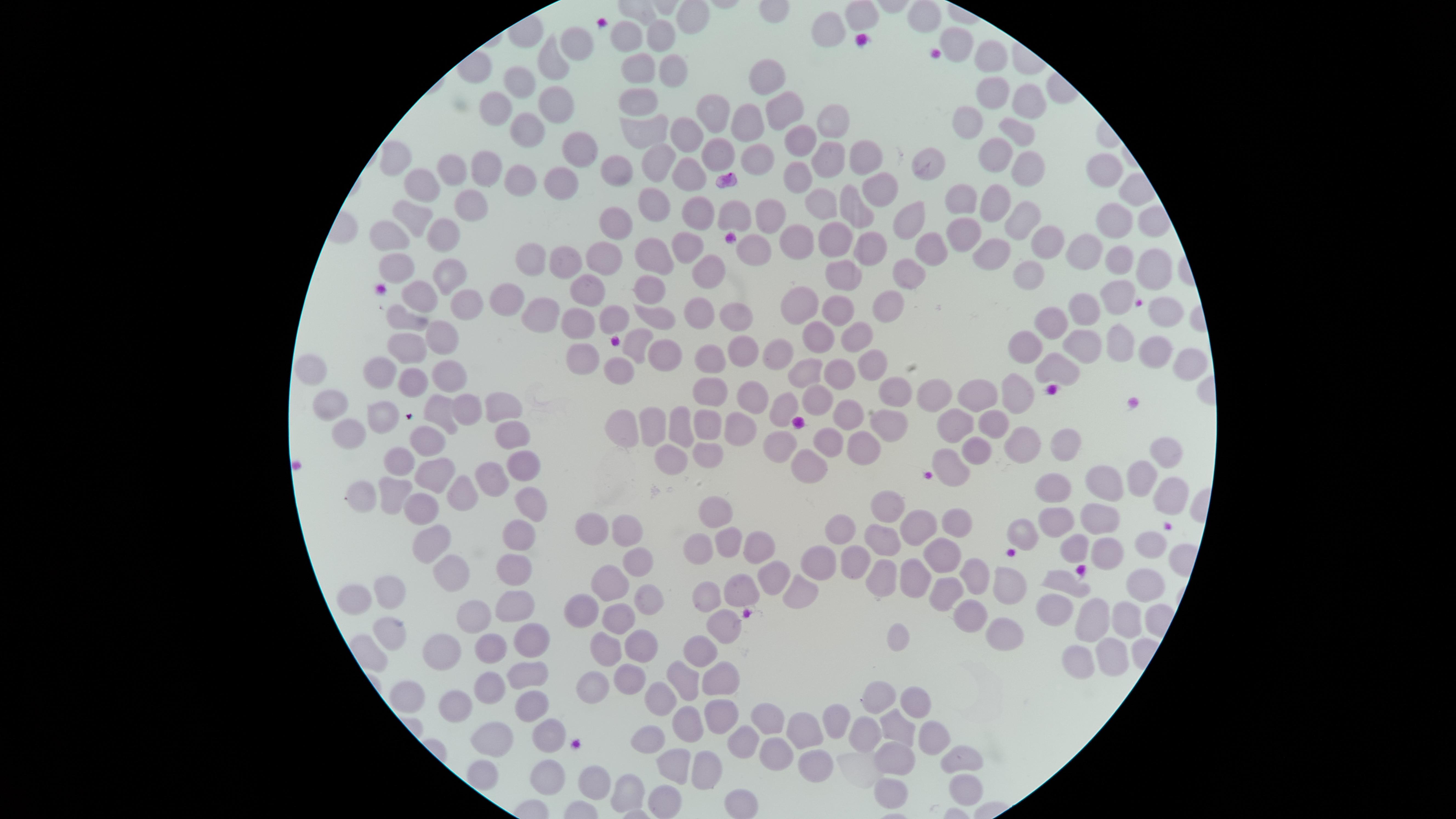

Approximate marker points, in pixels from the top-left corner. Uninfected RBCs: (x=860, y=16), (x=925, y=16), (x=663, y=37), (x=831, y=37), (x=633, y=38), (x=578, y=39), (x=958, y=40), (x=1004, y=50), (x=550, y=64), (x=641, y=67), (x=672, y=68), (x=771, y=79), (x=521, y=83), (x=992, y=91), (x=644, y=96), (x=548, y=103), (x=1030, y=103), (x=782, y=107), (x=495, y=110), (x=707, y=111), (x=828, y=118), (x=970, y=122), (x=743, y=123), (x=643, y=124), (x=686, y=127), (x=527, y=132), (x=1021, y=133), (x=797, y=144), (x=574, y=151), (x=861, y=154), (x=712, y=156), (x=991, y=156), (x=391, y=159), (x=825, y=159), (x=754, y=160), (x=482, y=162), (x=611, y=165), (x=661, y=165), (x=1027, y=165), (x=930, y=168), (x=1106, y=171), (x=447, y=173), (x=689, y=180), (x=793, y=181), (x=518, y=183), (x=561, y=189), (x=876, y=189), (x=421, y=190), (x=959, y=196), (x=654, y=200), (x=992, y=201), (x=819, y=204), (x=470, y=206), (x=696, y=210), (x=736, y=211), (x=855, y=212), (x=767, y=215), (x=418, y=218), (x=1014, y=218), (x=912, y=219), (x=611, y=223), (x=1114, y=227), (x=963, y=230), (x=833, y=237), (x=385, y=239), (x=439, y=239), (x=799, y=239), (x=1046, y=246), (x=686, y=247), (x=934, y=249), (x=1078, y=250), (x=865, y=251), (x=746, y=253), (x=992, y=253), (x=604, y=255), (x=1116, y=259), (x=652, y=260), (x=532, y=261), (x=563, y=262), (x=1153, y=268), (x=391, y=269), (x=910, y=271), (x=712, y=272), (x=444, y=274), (x=1027, y=274), (x=846, y=277), (x=650, y=285), (x=588, y=288), (x=1119, y=296), (x=420, y=299), (x=509, y=300), (x=464, y=301), (x=890, y=302), (x=798, y=306), (x=1089, y=306), (x=700, y=310), (x=837, y=310), (x=1166, y=310), (x=541, y=313), (x=403, y=318), (x=732, y=318), (x=657, y=319), (x=577, y=321), (x=1052, y=322), (x=820, y=336), (x=857, y=337), (x=441, y=340), (x=1122, y=342), (x=1089, y=343), (x=1026, y=344), (x=632, y=346), (x=406, y=348), (x=740, y=352), (x=665, y=356), (x=1154, y=356), (x=774, y=357), (x=710, y=358), (x=580, y=362), (x=1188, y=362), (x=1050, y=366), (x=378, y=368), (x=307, y=369), (x=875, y=369), (x=802, y=370), (x=620, y=373), (x=450, y=375), (x=843, y=376), (x=414, y=382), (x=1018, y=389), (x=899, y=390), (x=934, y=392), (x=981, y=394), (x=709, y=396), (x=757, y=397), (x=819, y=400), (x=330, y=405), (x=789, y=407), (x=465, y=408), (x=437, y=409), (x=501, y=409), (x=855, y=412), (x=383, y=413), (x=707, y=419), (x=676, y=422), (x=995, y=422), (x=622, y=423), (x=658, y=423), (x=954, y=424), (x=888, y=426), (x=346, y=430), (x=737, y=431), (x=511, y=434), (x=826, y=435), (x=425, y=440), (x=772, y=442), (x=867, y=444), (x=1064, y=444), (x=1020, y=445), (x=971, y=454), (x=1165, y=454), (x=663, y=457), (x=396, y=458), (x=516, y=460), (x=703, y=460), (x=799, y=463), (x=951, y=469), (x=488, y=473), (x=1139, y=473), (x=424, y=474), (x=1100, y=484), (x=463, y=486), (x=1051, y=488), (x=365, y=493), (x=1165, y=493), (x=390, y=495), (x=524, y=505), (x=414, y=510), (x=893, y=512), (x=707, y=515), (x=1051, y=520), (x=1097, y=521), (x=592, y=523), (x=957, y=524), (x=919, y=525), (x=626, y=527), (x=516, y=531), (x=841, y=532), (x=721, y=539), (x=877, y=541), (x=1150, y=541), (x=429, y=543), (x=1079, y=544), (x=697, y=546), (x=756, y=548), (x=1112, y=550), (x=940, y=555), (x=634, y=557), (x=815, y=559), (x=853, y=560), (x=510, y=569), (x=769, y=572), (x=878, y=574), (x=971, y=575), (x=442, y=579), (x=1061, y=579), (x=609, y=580), (x=915, y=580), (x=1143, y=584), (x=737, y=588), (x=1006, y=588), (x=389, y=590), (x=359, y=593), (x=946, y=593), (x=792, y=597), (x=701, y=598), (x=512, y=601), (x=1056, y=601), (x=643, y=602), (x=581, y=606), (x=472, y=614), (x=973, y=616), (x=1093, y=618), (x=1124, y=621), (x=616, y=622), (x=719, y=626), (x=1005, y=633), (x=388, y=635), (x=898, y=637), (x=526, y=642), (x=488, y=644), (x=601, y=646), (x=640, y=649), (x=700, y=650), (x=1112, y=654), (x=442, y=655), (x=1079, y=656), (x=522, y=670), (x=681, y=677), (x=626, y=678), (x=716, y=679), (x=487, y=686), (x=589, y=686), (x=410, y=689), (x=877, y=689), (x=663, y=692), (x=910, y=699), (x=453, y=701), (x=527, y=706), (x=713, y=709), (x=688, y=713), (x=767, y=713), (x=834, y=726), (x=895, y=728), (x=485, y=730), (x=551, y=730), (x=801, y=732), (x=865, y=733), (x=647, y=734), (x=930, y=735), (x=740, y=741), (x=776, y=750), (x=961, y=755), (x=671, y=761), (x=817, y=761), (x=898, y=761), (x=707, y=765), (x=545, y=772), (x=589, y=782), (x=968, y=789), (x=624, y=792), (x=891, y=794), (x=740, y=799), (x=660, y=801). One field of view of the specimen. Presence: no malaria parasites identified. Thin blood smear. Photographed with a smartphone camera through the microscope eyepiece. Circular visible region. Image is 1456×819 pixels. Giemsa-stained preparation.